Describe the morphology of the red blood cells.
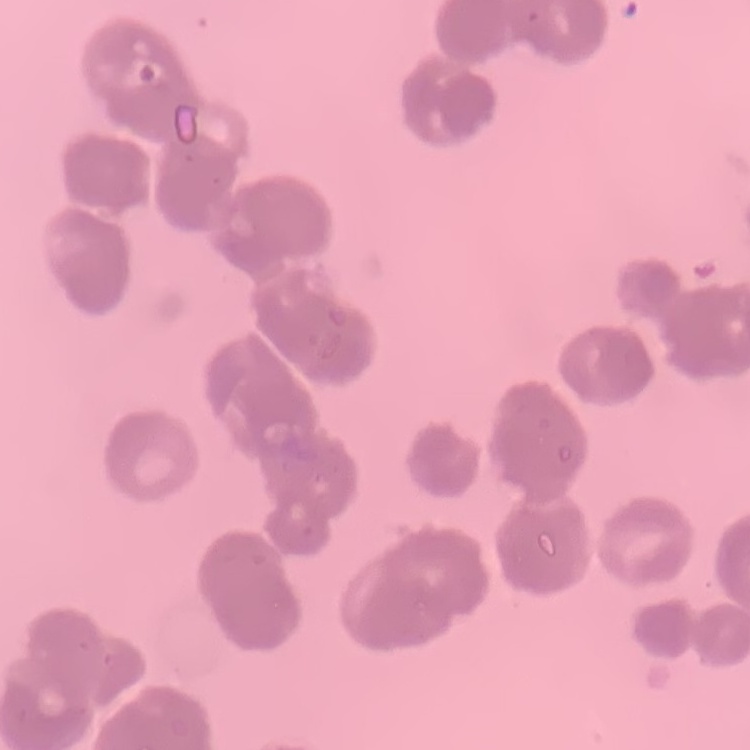

Rouleaux formation.

One tile cut from a larger photomicrograph. Thin peripheral smear. Stained with either Field's or Giemsa.